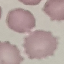
result = negative for malaria parasites
image type = automatically extracted cell patch, resized to 64 × 64 pixels
stain = Giemsa
preparation = thin smear
capture = smartphone through the microscope eyepiece